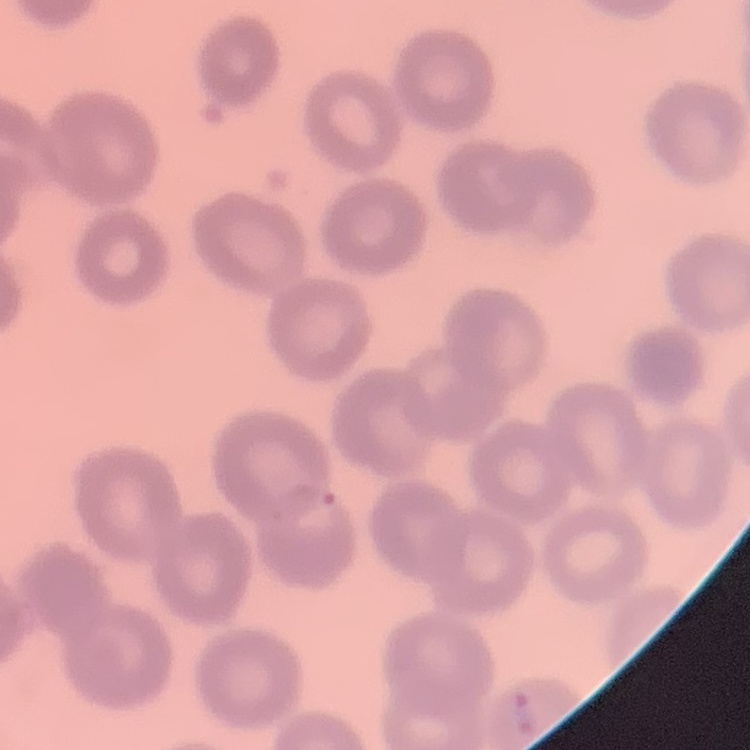
erythrocyte morphology = no rouleaux formation
stain = Field's or Giemsa
preparation = thin blood smear
image type = one tile cut from a larger photomicrograph